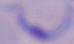

magnification = 1000x
identification = trypanosome
modality = micrograph